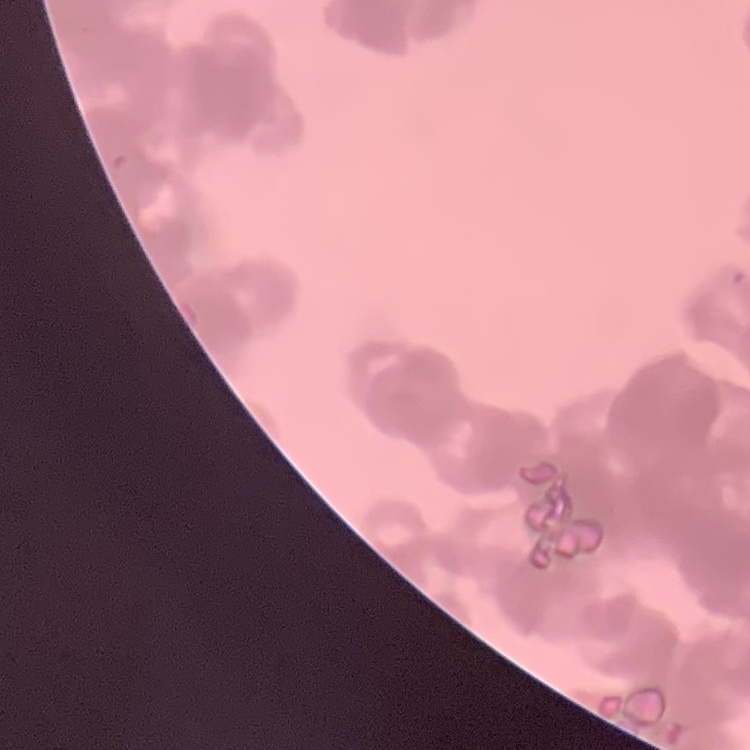

red blood cell morphology = rouleaux formation
preparation = thin blood film
image type = one tile cut from a larger photomicrograph
stain = Field's or Giemsa